Give the extent of all uninfected red blood cells.
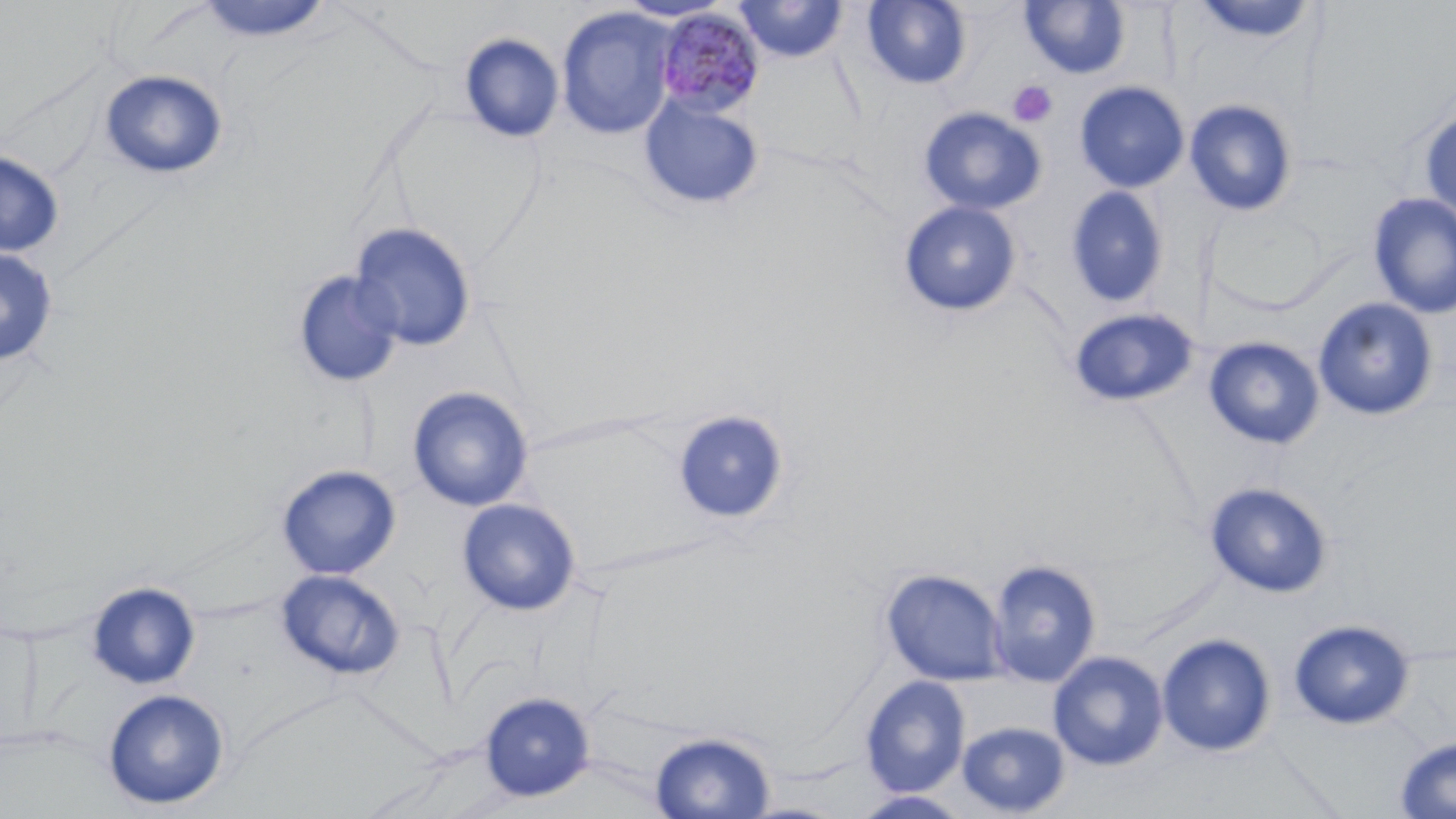
Approximate bounding boxes as named x1/y1/x2/y2 corners in pixels.
Uninfected red blood cells: (x1=862, y1=0, x2=971, y2=90), (x1=1189, y1=0, x2=1318, y2=46), (x1=196, y1=1, x2=334, y2=44), (x1=616, y1=1, x2=733, y2=23), (x1=733, y1=1, x2=849, y2=64), (x1=1019, y1=1, x2=1130, y2=79), (x1=556, y1=7, x2=678, y2=140), (x1=458, y1=32, x2=564, y2=143), (x1=99, y1=69, x2=228, y2=180), (x1=1074, y1=81, x2=1189, y2=193), (x1=638, y1=95, x2=765, y2=211), (x1=1184, y1=98, x2=1298, y2=217), (x1=918, y1=107, x2=1047, y2=216), (x1=1418, y1=108, x2=1456, y2=222), (x1=0, y1=150, x2=65, y2=258), (x1=1065, y1=186, x2=1170, y2=309), (x1=1367, y1=192, x2=1456, y2=318), (x1=898, y1=201, x2=1022, y2=318), (x1=348, y1=221, x2=477, y2=352), (x1=0, y1=247, x2=58, y2=366), (x1=293, y1=270, x2=404, y2=388), (x1=1312, y1=297, x2=1439, y2=421), (x1=1068, y1=307, x2=1200, y2=408), (x1=1203, y1=336, x2=1325, y2=450), (x1=407, y1=386, x2=534, y2=512), (x1=672, y1=410, x2=790, y2=526), (x1=277, y1=465, x2=401, y2=579), (x1=1204, y1=481, x2=1333, y2=598), (x1=456, y1=498, x2=581, y2=616), (x1=987, y1=559, x2=1102, y2=686), (x1=881, y1=568, x2=1006, y2=685), (x1=276, y1=569, x2=405, y2=681), (x1=86, y1=581, x2=200, y2=689), (x1=1289, y1=618, x2=1415, y2=729), (x1=1157, y1=633, x2=1276, y2=757), (x1=1047, y1=651, x2=1168, y2=771), (x1=860, y1=676, x2=970, y2=797), (x1=102, y1=688, x2=230, y2=810), (x1=479, y1=691, x2=595, y2=801), (x1=956, y1=720, x2=1070, y2=816), (x1=649, y1=730, x2=777, y2=818), (x1=1394, y1=736, x2=1456, y2=818), (x1=851, y1=791, x2=972, y2=819).

Summary:
  - Platelet locations: (x1=1008, y1=80, x2=1058, y2=128)
  - Plasmodium malariae-infected red blood cell locations: (x1=655, y1=9, x2=766, y2=119)
  - Slide-level diagnosis: Plasmodium malariae
  - Magnification: 1000x
  - Preparation: thin blood film
  - Modality: light microscopy
  - Field of view: single
  - Stain: May-Grünwald-Giemsa
  - Image size: 1456×819 pixels